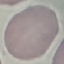
result = no malaria parasites detected
image type = automatically extracted cell patch, resized to 64 × 64 pixels
capture = smartphone through the microscope eyepiece
stain = Giemsa
preparation = thin blood film